Classify this cell by malaria status.
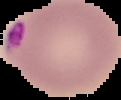
Parasitized.

Summary:
  - Image type: segmented cell region on a black background
  - Preparation: thin blood film
  - Image size: 121×100 pixels